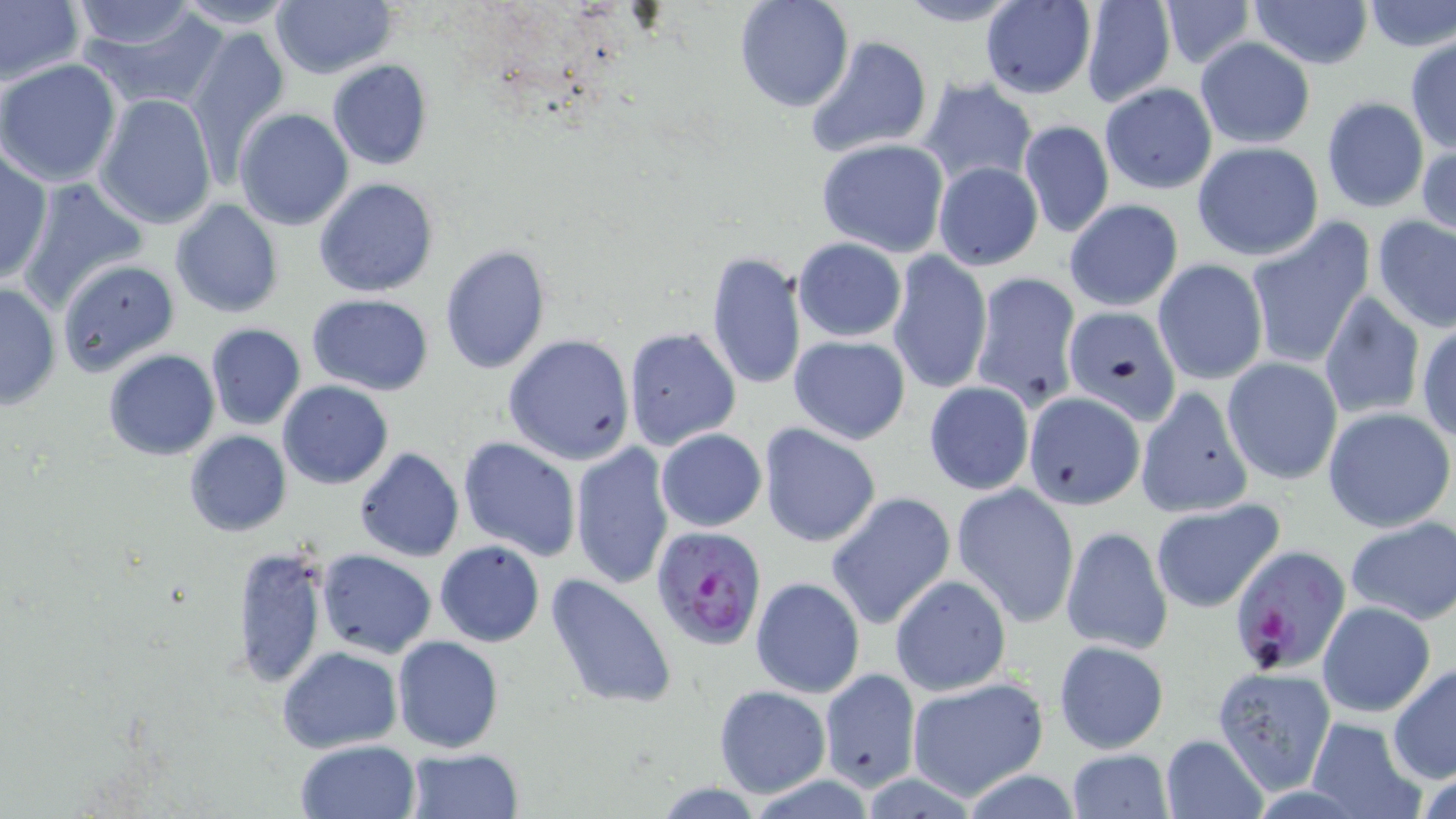
slide-level diagnosis = Plasmodium falciparum
field of view = one of a larger specimen
uninfected red blood cell locations = approximate bounding boxes as named x1/y1/x2/y2 corners in pixels: (x1=0, y1=0, x2=85, y2=89), (x1=733, y1=0, x2=854, y2=112), (x1=891, y1=0, x2=1026, y2=27), (x1=1155, y1=0, x2=1256, y2=68), (x1=1247, y1=0, x2=1373, y2=70), (x1=170, y1=1, x2=300, y2=30), (x1=269, y1=1, x2=398, y2=79), (x1=1359, y1=1, x2=1456, y2=51), (x1=68, y1=2, x2=208, y2=56), (x1=75, y1=2, x2=232, y2=111), (x1=979, y1=2, x2=1097, y2=98), (x1=1078, y1=4, x2=1176, y2=107), (x1=185, y1=24, x2=291, y2=168), (x1=805, y1=34, x2=934, y2=159), (x1=1405, y1=36, x2=1455, y2=154), (x1=1194, y1=37, x2=1316, y2=149), (x1=0, y1=59, x2=121, y2=187), (x1=326, y1=60, x2=434, y2=170), (x1=919, y1=77, x2=1037, y2=191), (x1=1100, y1=84, x2=1217, y2=193), (x1=95, y1=93, x2=217, y2=230), (x1=1321, y1=96, x2=1428, y2=213), (x1=233, y1=107, x2=354, y2=230), (x1=1018, y1=119, x2=1114, y2=239), (x1=1417, y1=137, x2=1455, y2=240), (x1=816, y1=138, x2=949, y2=257), (x1=1192, y1=142, x2=1325, y2=261), (x1=0, y1=150, x2=51, y2=286), (x1=933, y1=161, x2=1043, y2=270), (x1=18, y1=177, x2=147, y2=308), (x1=314, y1=177, x2=439, y2=297), (x1=1063, y1=198, x2=1183, y2=312), (x1=170, y1=200, x2=282, y2=318), (x1=1372, y1=215, x2=1456, y2=332), (x1=1244, y1=218, x2=1376, y2=371), (x1=793, y1=237, x2=907, y2=341), (x1=439, y1=245, x2=553, y2=375), (x1=705, y1=250, x2=808, y2=394), (x1=886, y1=251, x2=992, y2=397), (x1=1152, y1=258, x2=1268, y2=385), (x1=59, y1=259, x2=180, y2=374), (x1=970, y1=272, x2=1082, y2=411), (x1=0, y1=282, x2=61, y2=411), (x1=307, y1=293, x2=434, y2=396), (x1=1316, y1=293, x2=1426, y2=420), (x1=1061, y1=305, x2=1182, y2=425), (x1=1416, y1=322, x2=1456, y2=443), (x1=205, y1=324, x2=306, y2=431), (x1=624, y1=327, x2=741, y2=449), (x1=503, y1=334, x2=637, y2=465), (x1=788, y1=335, x2=911, y2=444), (x1=102, y1=348, x2=220, y2=461), (x1=1221, y1=357, x2=1343, y2=486), (x1=278, y1=380, x2=394, y2=488), (x1=923, y1=380, x2=1036, y2=496), (x1=1134, y1=386, x2=1251, y2=518), (x1=1022, y1=391, x2=1144, y2=510), (x1=1323, y1=406, x2=1454, y2=533), (x1=759, y1=423, x2=881, y2=547), (x1=655, y1=429, x2=767, y2=532), (x1=183, y1=430, x2=291, y2=535), (x1=458, y1=436, x2=580, y2=560), (x1=570, y1=441, x2=678, y2=590), (x1=354, y1=447, x2=464, y2=562), (x1=951, y1=482, x2=1080, y2=626), (x1=827, y1=492, x2=955, y2=630), (x1=1150, y1=498, x2=1284, y2=612), (x1=1344, y1=516, x2=1456, y2=626), (x1=1061, y1=525, x2=1173, y2=655), (x1=435, y1=540, x2=545, y2=647), (x1=235, y1=543, x2=328, y2=688), (x1=316, y1=550, x2=436, y2=658), (x1=545, y1=571, x2=678, y2=710), (x1=889, y1=574, x2=1012, y2=697), (x1=750, y1=576, x2=865, y2=699), (x1=1317, y1=600, x2=1435, y2=717), (x1=393, y1=636, x2=503, y2=752), (x1=1052, y1=639, x2=1169, y2=753), (x1=277, y1=646, x2=401, y2=752), (x1=1388, y1=665, x2=1456, y2=783), (x1=1213, y1=667, x2=1336, y2=793), (x1=820, y1=668, x2=922, y2=792), (x1=905, y1=677, x2=1048, y2=801), (x1=714, y1=684, x2=831, y2=797), (x1=1177, y1=702, x2=1310, y2=814), (x1=1305, y1=717, x2=1428, y2=818), (x1=1160, y1=734, x2=1269, y2=819), (x1=296, y1=740, x2=420, y2=818), (x1=406, y1=748, x2=523, y2=818), (x1=1064, y1=748, x2=1174, y2=818)
modality = light microscopy
Plasmodium falciparum-infected red blood cell locations = approximate bounding boxes as named x1/y1/x2/y2 corners in pixels: (x1=650, y1=524, x2=767, y2=650), (x1=1229, y1=546, x2=1351, y2=675)
magnification = 1000x
preparation = thin blood film
image size = 1456×819 pixels
stain = May-Grünwald-Giemsa